Assess this cell for malaria.
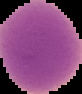

Uninfected.

From a thin blood film. Segmented cell region on a black background. Image is 82×94 pixels.